Classify this cell by malaria status.
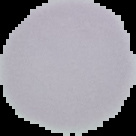
Uninfected.

Cell region segmented out of the field of view; the surrounding area is masked to black. From a thin blood film. Image is 136×136 pixels.